Identify the parasite.
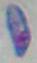
Toxoplasma gondii.

Summary:
  - Modality: micrograph
  - Magnification: 1000x